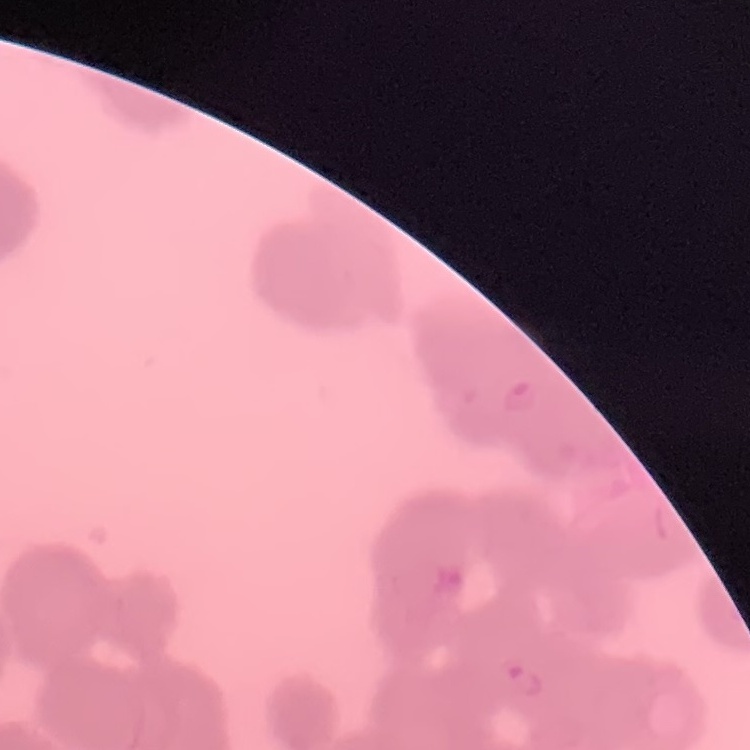
red blood cell morphology = rouleaux formation
preparation = thin blood film
stain = Field's or Giemsa
image type = square crop of a larger photomicrograph